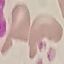

result = no malaria parasites seen
stain = Giemsa
image type = cell patch, automatically extracted from a larger field of view and resized to 64 × 64 pixels
capture = smartphone through the microscope eyepiece
preparation = thin blood smear